Report the malaria status of this cell.
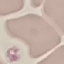
It is uninfected.

Cell patch, automatically extracted from a larger field of view and resized to 64 × 64 pixels. Photographed with a smartphone camera at the microscope eyepiece. Giemsa stain. Thin blood film.